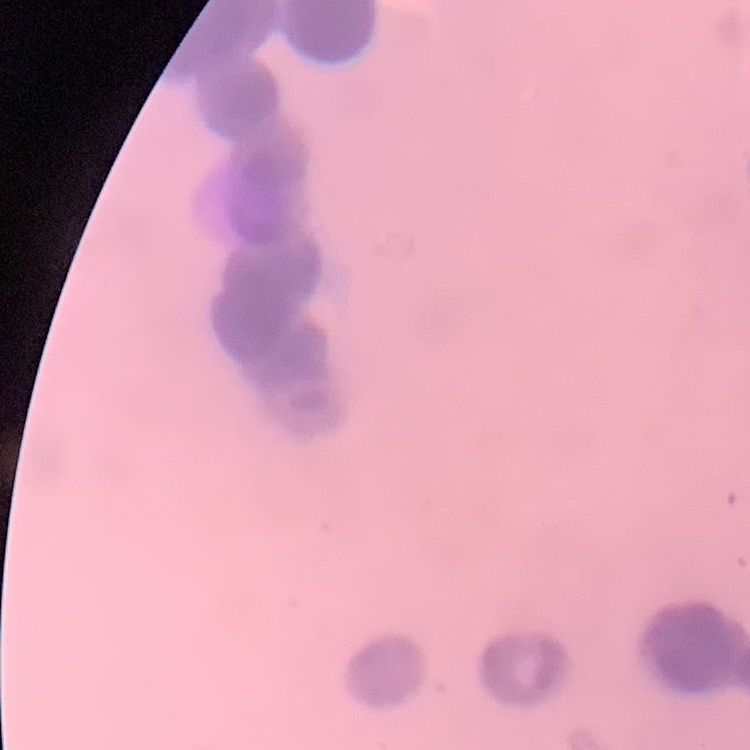
Summary:
  - Red blood cell morphology: rouleaux formation
  - Stain: Field's or Giemsa
  - Preparation: thin blood smear
  - Image type: square crop of a larger photomicrograph